Classify this cell by malaria status.
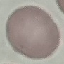

Uninfected.

Photographed with a smartphone camera at the microscope eyepiece. Automatically extracted cell patch, resized to 64 × 64 pixels. Giemsa stain. Thin blood film.